Report the malaria status of this cell.
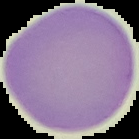

It is uninfected.

Image is 139×139 pixels. The area outside the segmented cell region is set to black. From a thin blood film.